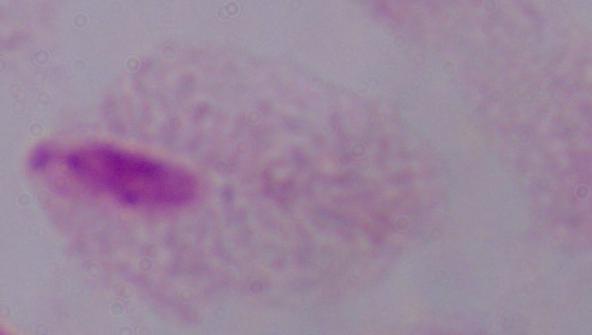
Summary:
  - Modality: photomicrograph
  - Identification: trichomonad
  - Magnification: 1000x